Assess the morphology of the red blood cells.
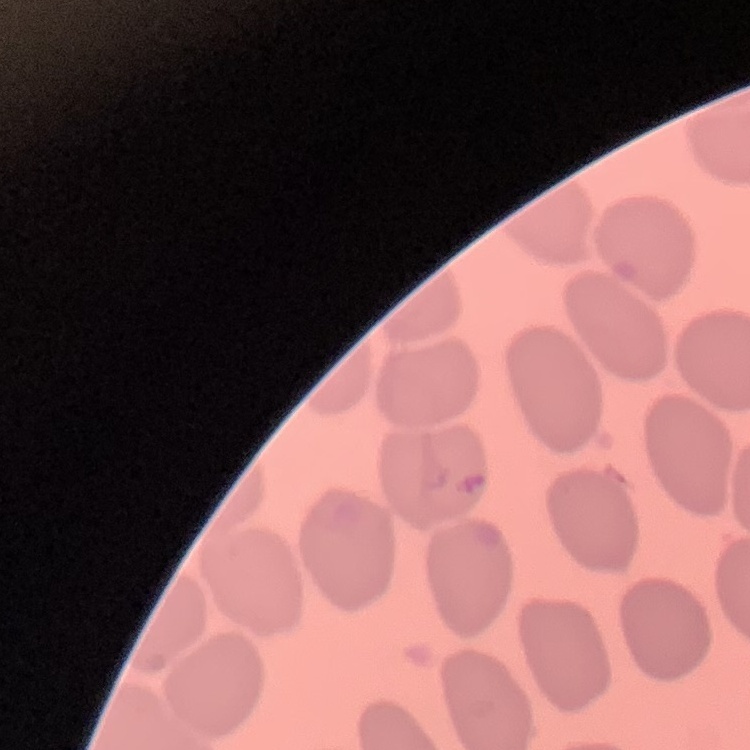
No rouleaux formation.

One tile cut from a larger photomicrograph. Field's or Giemsa stain. Thin blood film.